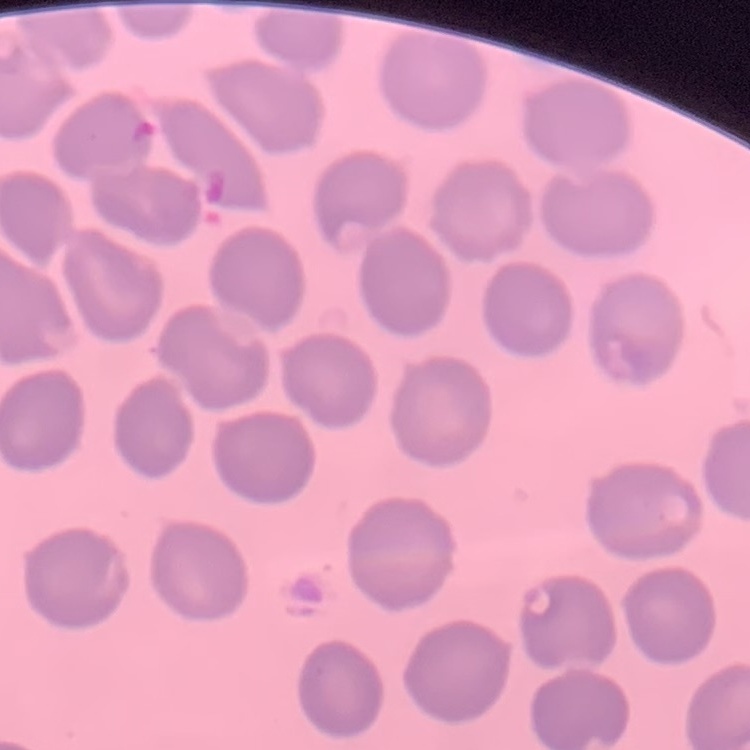

erythrocyte_morphology: no rouleaux formation
stain: Field's or Giemsa
image_type: one tile cut from a larger photomicrograph
preparation: thin blood smear